Assess this cell for malaria.
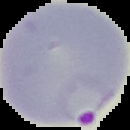

Parasitized.

From a thin blood film. Cell region segmented out of the field of view; the surrounding area is masked to black. Image is 130×130 pixels.